Report the malaria status of this cell.
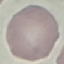

It is uninfected.

image type = cell patch, automatically extracted from a larger field of view and resized to 64 × 64 pixels
preparation = thin blood film
capture = smartphone camera at the microscope eyepiece
stain = Giemsa